Name the cell type shown.
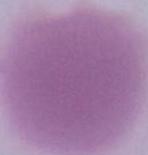

An erythrocyte.

magnification = 1000x
modality = photomicrograph